Give the extent of all Plasmodium falciparum-infected red blood cells.
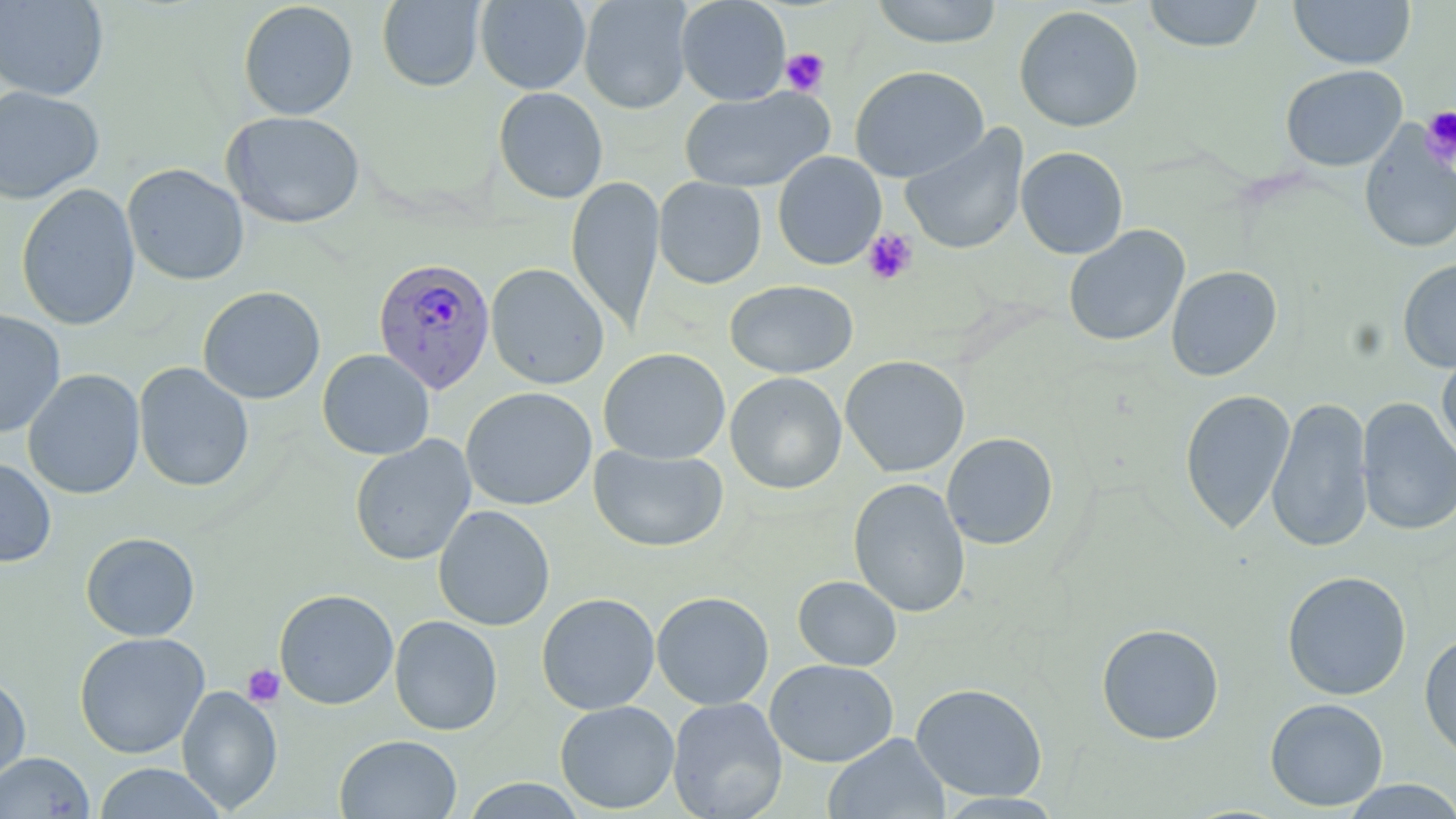

Approximate bounding boxes as (x1,y1)-(x2,y2) corner pairs in pixels.
Plasmodium falciparum-infected red blood cells: (373,257)-(496,393).

slide-level diagnosis = Plasmodium falciparum
image size = 1456×819 pixels
platelet locations = approximate bounding boxes as (x1,y1)-(x2,y2) corner pairs in pixels: (781,48)-(829,95), (1421,107)-(1456,168), (862,228)-(918,286), (242,665)-(285,707)
magnification = 1000x
modality = optical microscopy
stain = May-Grünwald-Giemsa
preparation = thin blood film
uninfected red blood cell locations = approximate bounding boxes as (x1,y1)-(x2,y2) corner pairs in pixels: (578,0)-(693,114), (676,0)-(791,105), (869,0)-(1004,49), (1143,0)-(1265,52), (1288,0)-(1416,69), (0,1)-(109,101), (238,1)-(358,120), (377,1)-(485,91), (475,1)-(591,94), (1014,5)-(1144,133), (850,65)-(989,183), (1280,65)-(1407,171), (0,85)-(104,204), (493,87)-(608,204), (679,87)-(834,194), (222,110)-(366,229), (899,124)-(1029,256), (1359,124)-(1456,254), (1016,146)-(1129,259), (772,151)-(886,270), (122,163)-(249,286), (566,175)-(665,334), (654,177)-(767,289), (16,183)-(141,331), (1063,225)-(1190,347), (1397,259)-(1456,373), (486,263)-(609,389), (1166,265)-(1282,381), (724,280)-(858,379), (198,285)-(326,404), (0,309)-(66,439), (1437,347)-(1456,464), (598,348)-(730,464), (318,349)-(434,460), (840,355)-(970,478), (133,362)-(254,492), (23,369)-(146,500), (725,372)-(847,495), (460,387)-(597,510), (1179,389)-(1295,535), (1267,395)-(1373,553), (1357,397)-(1456,537), (941,432)-(1059,550), (350,435)-(475,566), (589,445)-(728,553), (0,456)-(57,568), (848,478)-(971,618), (433,504)-(555,631), (80,532)-(201,642), (1282,571)-(1412,700), (792,575)-(902,671), (273,589)-(399,710), (651,591)-(774,710), (536,592)-(660,715), (389,615)-(503,736), (1096,623)-(1224,745), (73,632)-(210,759), (1419,632)-(1456,764), (764,659)-(899,767), (0,672)-(31,787), (910,682)-(1048,801), (176,685)-(283,814), (667,696)-(788,819), (1265,697)-(1388,812), (554,700)-(680,814), (823,733)-(949,819), (334,734)-(462,819), (0,751)-(95,818), (92,762)-(227,819), (461,778)-(587,818), (1339,780)-(1456,818)
field of view = single